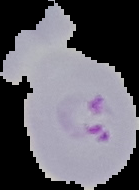

image_type: segmented cell region with the area outside set to black
image_size: 139×190 pixels
preparation: thin blood smear
malaria_status: parasitized